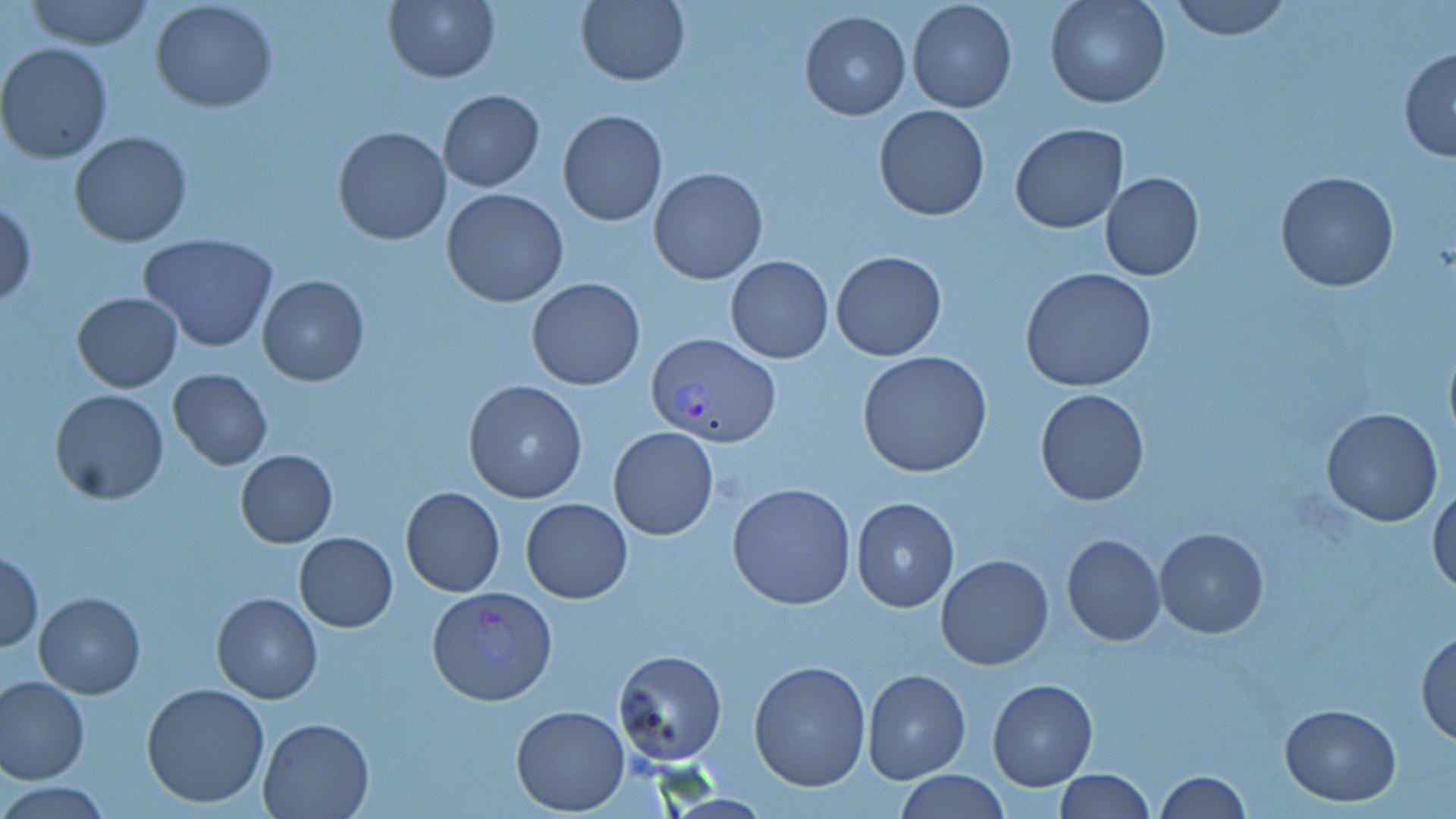

Approximate bounding boxes as named x1/y1/x2/y2 corners in pixels. Uninfected red blood cell locations: (x1=23, y1=0, x2=157, y2=51), (x1=1045, y1=0, x2=1169, y2=108), (x1=1167, y1=0, x2=1290, y2=39), (x1=384, y1=1, x2=499, y2=82), (x1=575, y1=1, x2=690, y2=85), (x1=906, y1=1, x2=1017, y2=113), (x1=150, y1=2, x2=278, y2=113), (x1=800, y1=9, x2=911, y2=120), (x1=0, y1=43, x2=114, y2=163), (x1=1398, y1=48, x2=1456, y2=161), (x1=438, y1=89, x2=545, y2=192), (x1=873, y1=104, x2=991, y2=221), (x1=558, y1=109, x2=667, y2=226), (x1=1010, y1=124, x2=1127, y2=232), (x1=331, y1=126, x2=451, y2=244), (x1=69, y1=130, x2=192, y2=247), (x1=648, y1=168, x2=767, y2=283), (x1=1100, y1=171, x2=1204, y2=281), (x1=1276, y1=171, x2=1399, y2=293), (x1=441, y1=188, x2=569, y2=308), (x1=0, y1=200, x2=37, y2=307), (x1=138, y1=233, x2=278, y2=353), (x1=830, y1=249, x2=947, y2=361), (x1=725, y1=256, x2=833, y2=363), (x1=1020, y1=268, x2=1159, y2=394), (x1=257, y1=275, x2=370, y2=387), (x1=527, y1=276, x2=646, y2=390), (x1=72, y1=291, x2=183, y2=392), (x1=1442, y1=334, x2=1456, y2=449), (x1=858, y1=350, x2=992, y2=478), (x1=169, y1=368, x2=272, y2=469), (x1=463, y1=380, x2=588, y2=504), (x1=49, y1=388, x2=169, y2=504), (x1=1035, y1=388, x2=1151, y2=505), (x1=1321, y1=408, x2=1444, y2=527), (x1=608, y1=427, x2=718, y2=540), (x1=236, y1=449, x2=337, y2=547), (x1=1429, y1=480, x2=1456, y2=597), (x1=727, y1=482, x2=856, y2=609), (x1=401, y1=486, x2=505, y2=597), (x1=851, y1=497, x2=961, y2=613), (x1=521, y1=498, x2=632, y2=603), (x1=1154, y1=526, x2=1269, y2=638), (x1=294, y1=532, x2=398, y2=631), (x1=1061, y1=534, x2=1166, y2=646), (x1=1, y1=551, x2=44, y2=650), (x1=935, y1=555, x2=1054, y2=670), (x1=34, y1=591, x2=145, y2=698), (x1=211, y1=592, x2=322, y2=703), (x1=1415, y1=628, x2=1456, y2=744), (x1=612, y1=650, x2=726, y2=765), (x1=749, y1=659, x2=870, y2=792), (x1=862, y1=668, x2=971, y2=783), (x1=0, y1=675, x2=89, y2=782), (x1=987, y1=678, x2=1098, y2=791), (x1=141, y1=682, x2=270, y2=808), (x1=1279, y1=702, x2=1403, y2=805), (x1=511, y1=704, x2=630, y2=814), (x1=258, y1=717, x2=374, y2=818), (x1=1053, y1=769, x2=1156, y2=819), (x1=898, y1=771, x2=1007, y2=819), (x1=1154, y1=771, x2=1252, y2=817), (x1=3, y1=781, x2=115, y2=816). Plasmodium vivax-infected red blood cell locations: (x1=647, y1=333, x2=782, y2=448), (x1=428, y1=586, x2=558, y2=705). Slide-level diagnosis: Plasmodium vivax. May-Grünwald-Giemsa-stained preparation. Image is 1456×819 pixels. Captured at 1000x magnification. Thin blood smear. Optical microscopy. One field of a larger specimen.